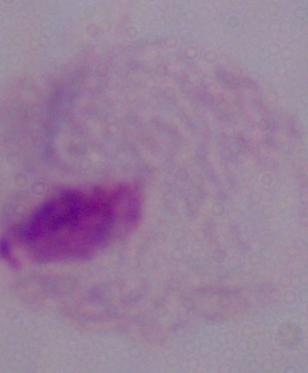 Micrograph. A trichomonad is seen. Captured at 1000x magnification.